Point out each Plasmodium parasite.
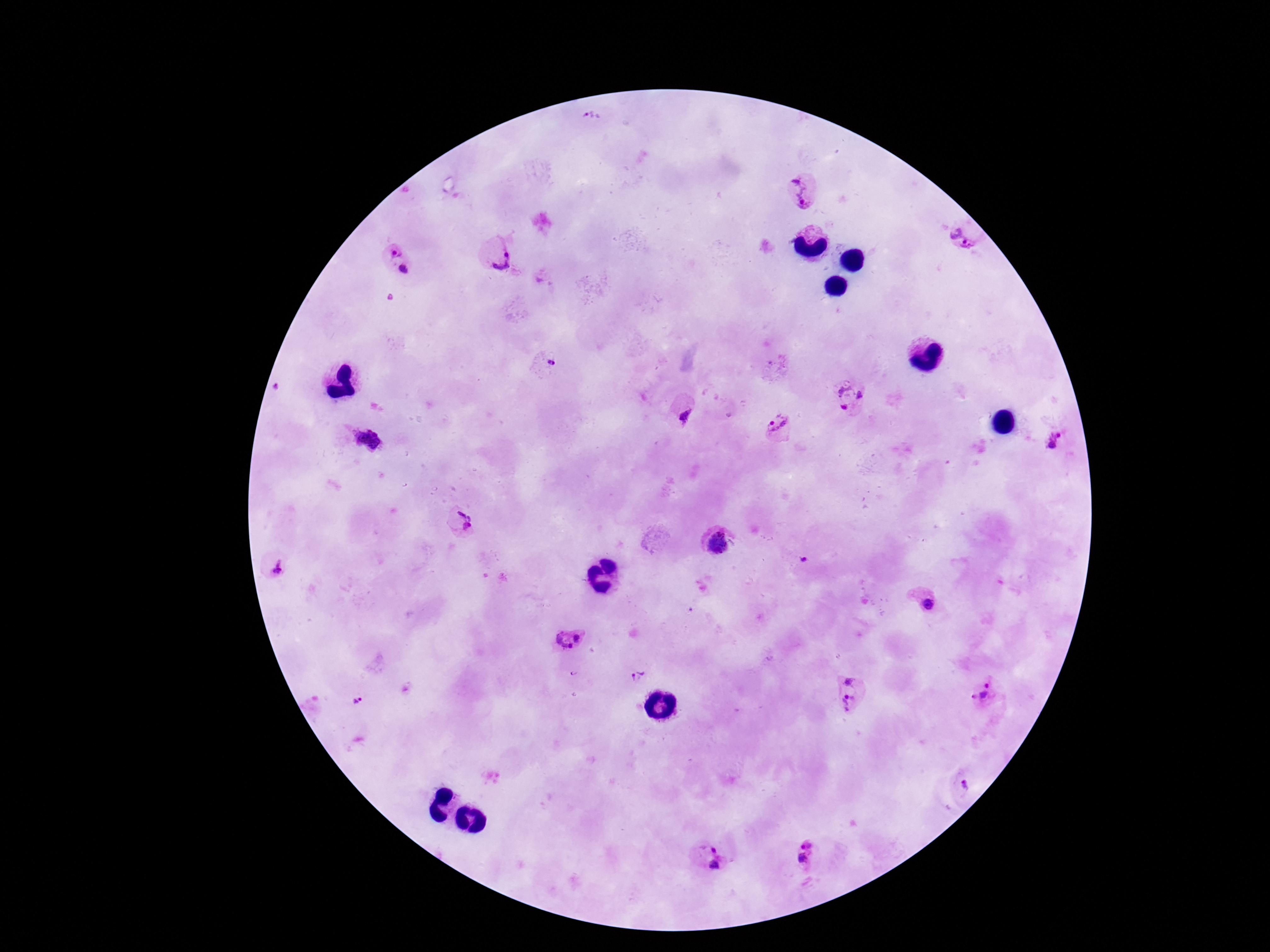
Approximate centers as {x, y} in pixels.
Plasmodium parasites: {593, 116}, {803, 194}, {962, 239}, {395, 251}, {500, 258}, {403, 269}, {391, 297}, {547, 363}, {849, 397}, {686, 413}, {777, 426}, {364, 439}, {1056, 442}, {462, 520}, {718, 543}, {279, 567}, {927, 604}, {568, 638}, {575, 672}, {637, 677}, {848, 680}, {987, 684}, {978, 696}, {848, 700}, {358, 701}, {964, 787}, {806, 853}, {708, 857}.

magnification = 100x
image size = 1270×952 pixels
field of view = single
stain = Giemsa
patient malaria status = positive
capture = smartphone camera through the microscope eyepiece
preparation = thick blood smear